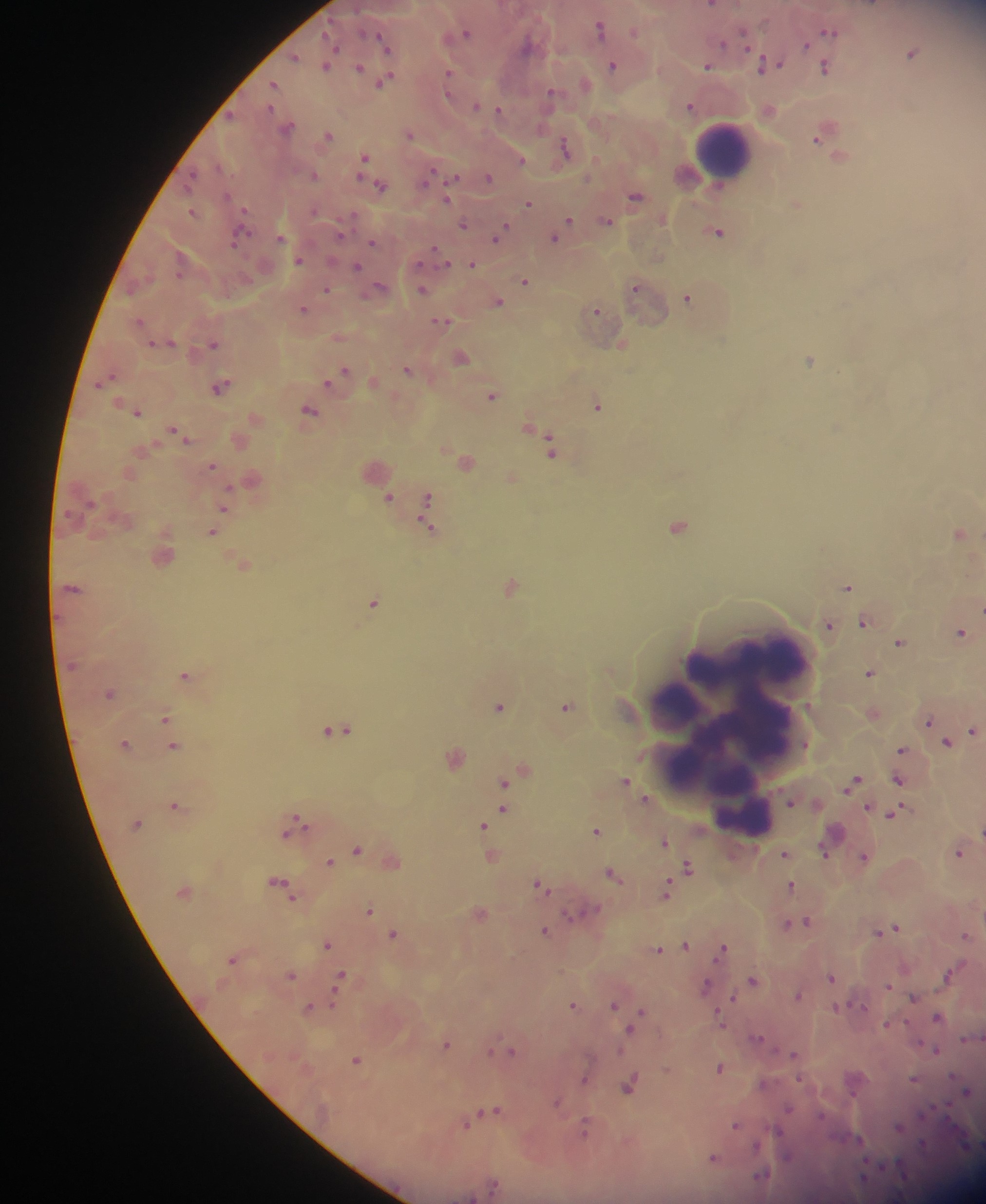

image_size: 986×1204 pixels
field_of_view: single
capture: mobile-phone photograph through a microscope
leukocyte_locations: 'approximate centers as (x, y) in pixels: (725, 146), (730, 726)'
malaria_parasite_locations: 'approximate centers as (x, y) in pixels: (599, 27), (743, 31), (830, 31), (467, 34), (382, 40), (724, 43), (807, 44), (385, 45), (338, 48), (748, 48), (913, 52), (294, 55), (779, 63), (325, 64), (762, 65), (361, 66), (614, 66), (708, 66), (826, 66), (451, 71), (585, 82), (274, 83), (550, 93), (477, 107), (499, 109), (330, 134), (816, 140), (566, 146), (365, 157), (520, 160), (193, 173), (315, 174), (432, 174), (489, 176), (455, 177), (378, 184), (636, 195), (529, 203), (244, 209), (191, 212), (569, 220), (607, 220), (464, 224), (505, 226), (500, 231), (719, 233), (556, 235), (280, 237), (371, 244), (233, 246), (438, 252), (300, 259), (446, 263), (473, 263), (420, 264), (357, 265), (178, 275), (525, 280), (327, 288), (636, 288), (424, 290), (687, 297), (499, 303), (304, 309), (598, 309), (443, 321), (153, 341), (214, 342), (347, 368), (408, 368), (111, 375), (224, 383), (329, 383), (494, 395), (596, 407), (138, 412), (173, 430), (542, 435), (187, 441), (212, 466), (230, 486), (389, 495), (429, 497), (224, 509), (426, 526), (212, 534), (510, 587), (847, 587), (374, 603), (865, 621), (965, 632), (901, 641), (186, 674), (871, 674), (500, 706), (566, 706), (166, 717), (930, 721), (337, 730), (973, 731), (948, 742), (174, 745), (805, 745), (903, 749), (524, 770), (899, 779), (626, 780), (503, 784), (638, 790), (645, 798), (174, 806), (869, 806), (503, 808), (897, 812), (295, 814), (136, 824), (483, 824), (308, 826), (596, 831), (286, 834), (665, 840), (358, 849), (961, 851), (825, 852), (784, 854), (864, 857), (331, 862), (688, 865), (610, 873), (279, 880), (539, 883), (791, 884), (667, 885), (544, 887), (295, 897), (597, 908), (369, 910), (568, 916), (790, 923), (808, 923), (893, 928), (544, 929), (882, 931), (393, 933), (967, 935), (327, 943), (686, 945), (723, 945), (660, 951), (233, 960), (342, 972), (292, 974), (948, 975), (831, 978), (754, 980), (889, 985), (708, 987), (798, 995), (915, 996), (733, 997), (574, 1003), (615, 1004), (332, 1005), (865, 1006), (308, 1007), (837, 1008), (640, 1010), (717, 1013), (938, 1016), (908, 1020), (887, 1023), (722, 1026), (631, 1028), (758, 1039), (447, 1044), (513, 1049), (620, 1050), (936, 1050), (490, 1051), (792, 1054), (358, 1059), (721, 1068), (667, 1070), (800, 1077), (914, 1077), (953, 1077), (585, 1080), (629, 1088), (967, 1092), (558, 1102), (947, 1104), (499, 1109), (789, 1109), (481, 1112), (924, 1115), (586, 1117), (822, 1117), (738, 1124), (466, 1125), (900, 1126), (775, 1128), (780, 1131), (587, 1134), (630, 1141), (924, 1144), (757, 1146), (788, 1156), (714, 1158), (761, 1175), (494, 1187)'
preparation: thick blood smear
country: Ghana